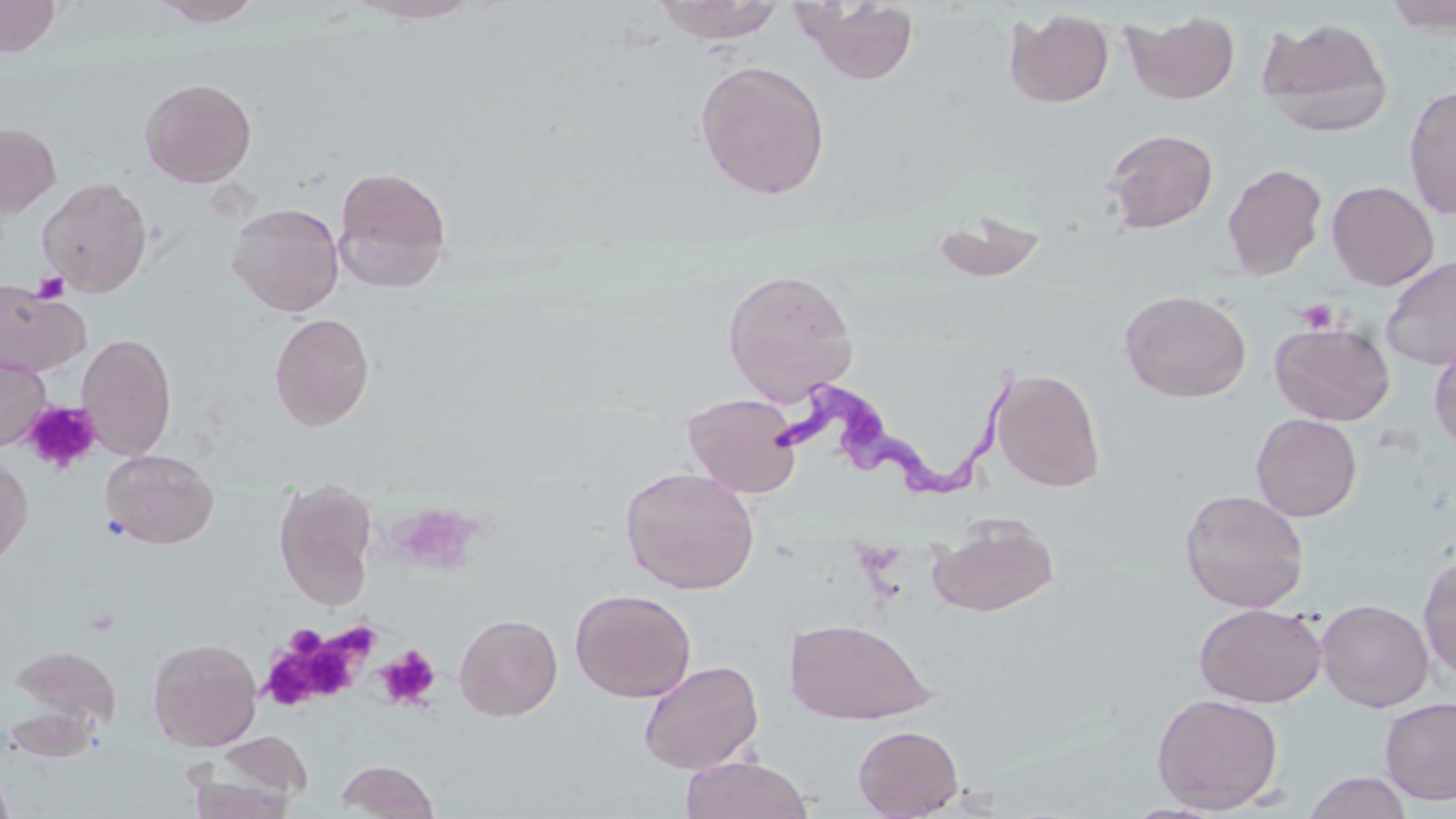

Approximate bounding boxes as [x1, y1, x2, y2] in pixels. Uninfected red blood cell locations: [0, 0, 61, 57], [150, 0, 265, 27], [347, 0, 487, 25], [1382, 0, 1456, 36], [652, 1, 786, 45], [792, 1, 921, 84], [1005, 8, 1114, 108], [1122, 9, 1241, 105], [1257, 17, 1393, 137], [694, 60, 831, 199], [139, 77, 257, 187], [1403, 85, 1456, 220], [0, 122, 61, 217], [1103, 128, 1218, 233], [1222, 163, 1327, 281], [332, 165, 453, 292], [37, 177, 153, 297], [1327, 180, 1439, 290], [1355, 192, 1453, 358], [227, 202, 344, 317], [932, 211, 1048, 283], [1380, 256, 1456, 371], [722, 268, 859, 403], [0, 279, 91, 377], [1119, 289, 1251, 403], [269, 312, 376, 431], [1270, 321, 1394, 426], [77, 332, 176, 462], [1429, 339, 1456, 455], [0, 352, 51, 451], [989, 367, 1106, 492], [682, 393, 803, 498], [1251, 413, 1362, 521], [100, 449, 219, 549], [0, 451, 34, 567], [620, 466, 760, 594], [274, 477, 379, 609], [1179, 488, 1310, 614], [928, 515, 1060, 618], [1418, 551, 1456, 680], [570, 588, 697, 702], [1316, 599, 1434, 711], [1194, 603, 1327, 707], [454, 613, 563, 721], [784, 618, 934, 725], [148, 636, 262, 751], [8, 643, 123, 732], [639, 659, 764, 775], [1152, 692, 1284, 813], [1379, 696, 1456, 806], [853, 724, 964, 818], [213, 731, 314, 807], [679, 755, 814, 819], [336, 760, 440, 818], [0, 765, 15, 819], [186, 765, 301, 819], [1302, 771, 1413, 818]. Platelet locations: [31, 271, 70, 304], [1295, 299, 1341, 334], [22, 400, 101, 474], [264, 626, 372, 710], [374, 645, 442, 710]. Trypanosoma brucei locations: [771, 369, 1030, 503]. Slide-level diagnosis: Trypanosoma brucei. Image is 1456×819 pixels. One field of a larger specimen. May-Grünwald-Giemsa-stained preparation. Thin blood film. 1000x magnification. Optical microscopy.